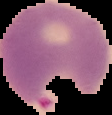

image size = 112×115 pixels
image type = segmented cell region with the area outside set to black
result = Plasmodium parasites detected
preparation = thin blood film